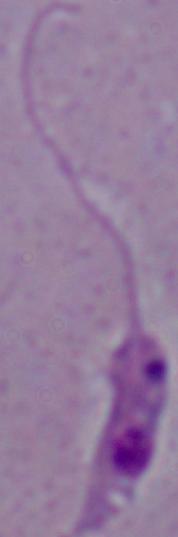
Summary:
  - Identification: Leishmania
  - Magnification: 1000x
  - Modality: micrograph